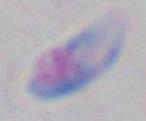

Micrograph. 1000x magnification. Toxoplasma gondii is seen.